State which parasite is depicted.
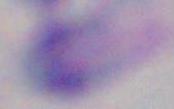

This is Toxoplasma gondii.

Photomicrograph. 1000x magnification.